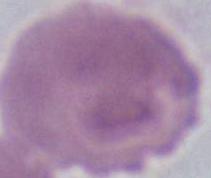

A red blood cell is shown. Micrograph. Captured at 1000x magnification.